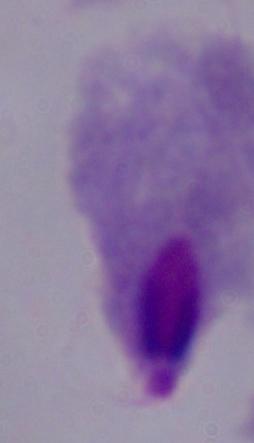

{
  "identification": "trichomonad",
  "modality": "micrograph",
  "magnification": "1000x"
}